Comment on the morphology of the red blood cells.
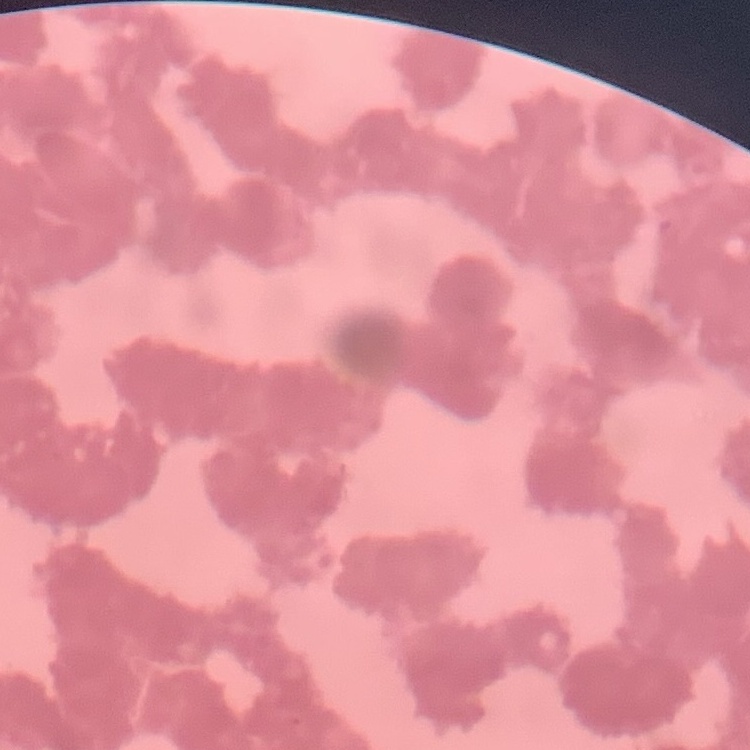

Rouleaux formation.

image type = one tile cut from a larger photomicrograph
stain = Field's or Giemsa
preparation = thin blood film